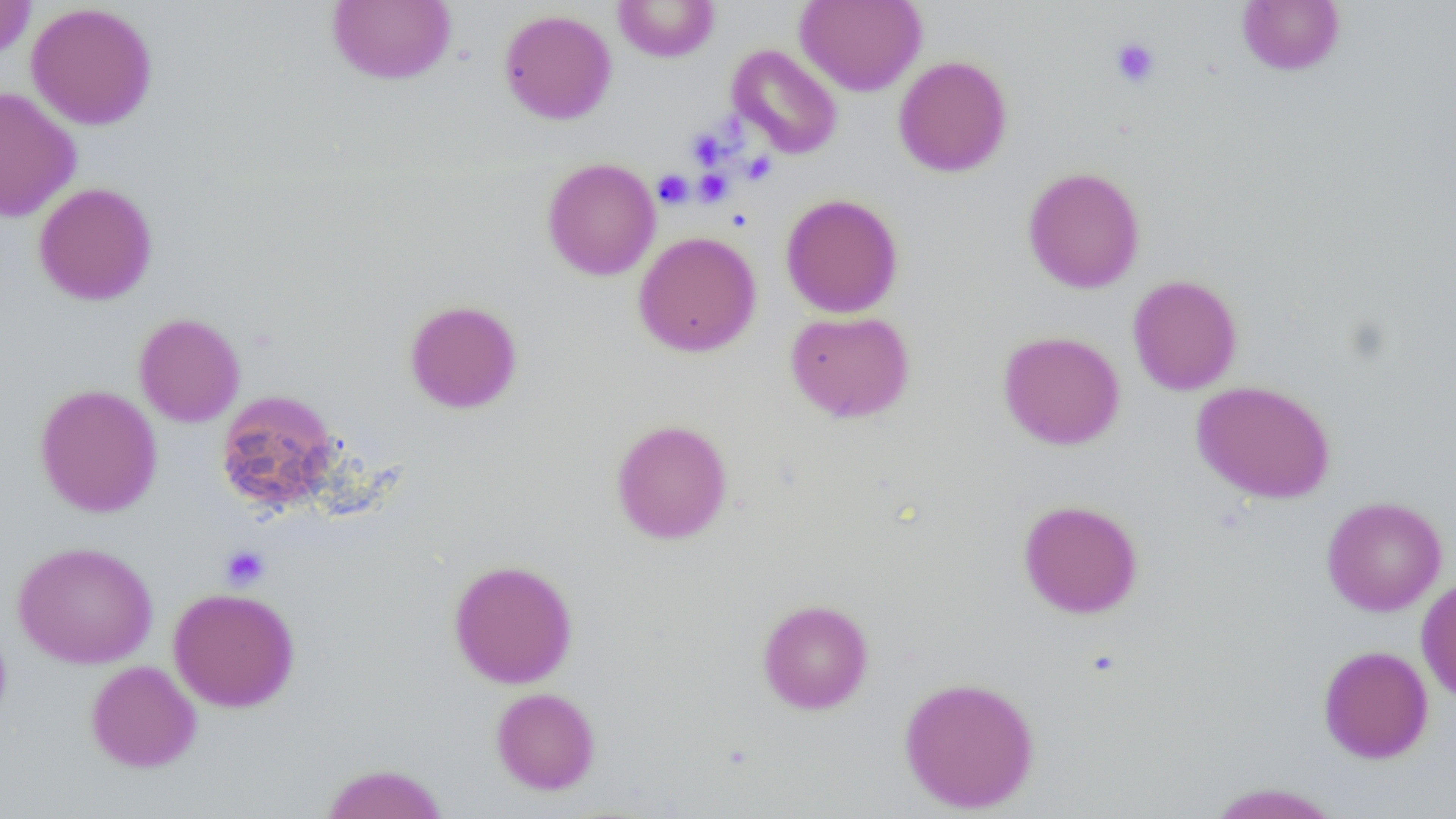 Approximate bounding boxes as [x1, y1, x2, y2] in pixels. Uninfected red blood cell locations: [0, 0, 36, 60], [327, 0, 456, 85], [612, 0, 720, 62], [795, 0, 926, 96], [1237, 1, 1345, 75], [26, 2, 158, 130], [498, 9, 617, 125], [727, 44, 843, 159], [894, 56, 1012, 177], [0, 87, 82, 222], [542, 158, 661, 280], [1022, 166, 1145, 293], [32, 182, 158, 305], [780, 193, 904, 318], [633, 231, 762, 357], [1128, 275, 1243, 395], [404, 299, 523, 414], [785, 310, 915, 423], [134, 313, 245, 427], [997, 331, 1125, 450], [1191, 380, 1336, 504], [35, 384, 162, 517], [215, 389, 342, 514], [611, 418, 733, 544], [1322, 496, 1447, 616], [1017, 499, 1143, 618], [12, 541, 158, 668], [448, 559, 578, 689], [1416, 577, 1456, 703], [168, 587, 301, 712], [757, 599, 874, 714], [0, 619, 12, 732], [1317, 645, 1434, 764], [85, 660, 202, 772], [899, 676, 1040, 813], [490, 687, 601, 795], [320, 762, 449, 819], [1206, 782, 1345, 819]. Platelet locations: [1110, 37, 1161, 89], [687, 129, 726, 168], [741, 150, 776, 185], [694, 168, 733, 206], [653, 169, 693, 209], [220, 545, 270, 590]. Slide-level diagnosis: negative for blood parasites. Image is 1456×819 pixels. 1000x magnification. Single field of view. Light microscopy. Thin blood film.